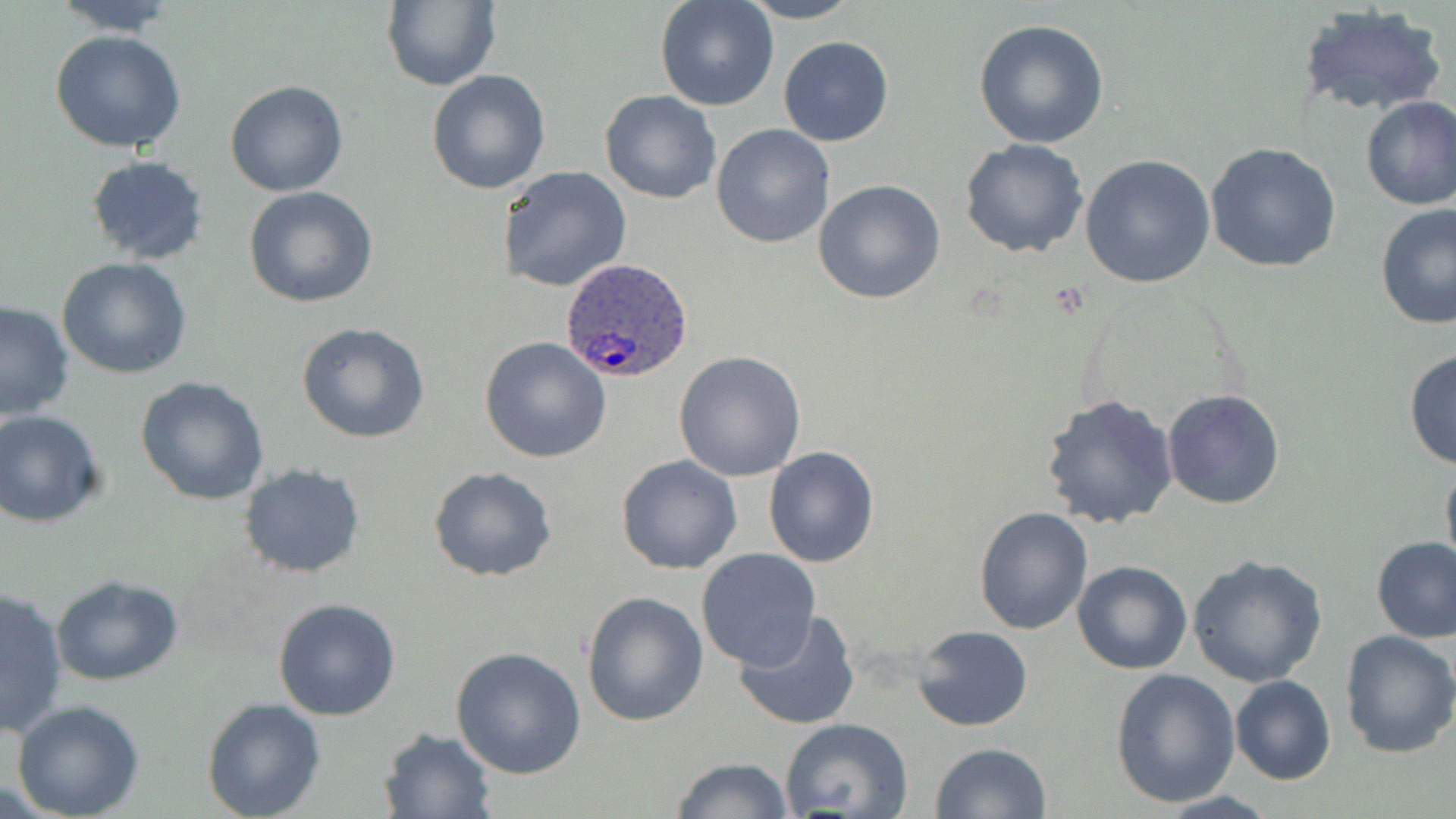
Approximate bounding boxes as [x1, y1, x2, y2] in pixels. Uninfected red blood cell locations: [50, 0, 182, 36], [383, 0, 501, 92], [740, 0, 862, 23], [654, 1, 778, 111], [1296, 4, 1446, 119], [972, 18, 1109, 150], [49, 30, 188, 153], [778, 36, 893, 147], [425, 69, 549, 195], [224, 80, 349, 197], [599, 90, 721, 204], [1359, 96, 1456, 211], [710, 124, 835, 248], [961, 138, 1089, 258], [1205, 142, 1342, 273], [1082, 153, 1217, 288], [85, 154, 209, 265], [499, 165, 632, 292], [813, 179, 946, 303], [243, 186, 379, 308], [1376, 204, 1456, 331], [57, 256, 192, 379], [0, 300, 77, 420], [297, 322, 432, 443], [480, 335, 612, 463], [1403, 348, 1456, 471], [673, 350, 806, 482], [136, 376, 270, 505], [1161, 389, 1285, 511], [1040, 392, 1179, 529], [0, 409, 108, 528], [764, 446, 881, 567], [616, 455, 742, 575], [1440, 455, 1456, 580], [239, 464, 366, 579], [428, 466, 557, 582], [974, 507, 1092, 633], [1372, 538, 1456, 642], [696, 548, 820, 668], [1188, 555, 1328, 687], [1073, 561, 1191, 675], [48, 575, 187, 687], [0, 586, 70, 735], [581, 591, 709, 726], [273, 597, 402, 720], [732, 611, 861, 731], [914, 626, 1033, 730], [1338, 630, 1456, 757], [450, 646, 586, 779], [1109, 667, 1241, 807], [1229, 674, 1336, 785], [10, 699, 146, 819], [203, 699, 326, 819], [782, 718, 915, 818], [377, 725, 497, 818], [930, 742, 1053, 819], [671, 757, 793, 817]. Plasmodium ovale-infected red blood cell locations: [561, 258, 695, 383]. Slide-level diagnosis: Plasmodium ovale. Image is 1456×819 pixels. Optical microscopy. One field of a larger specimen. Thin blood film. May-Grünwald-Giemsa stain. Captured at 1000x magnification.